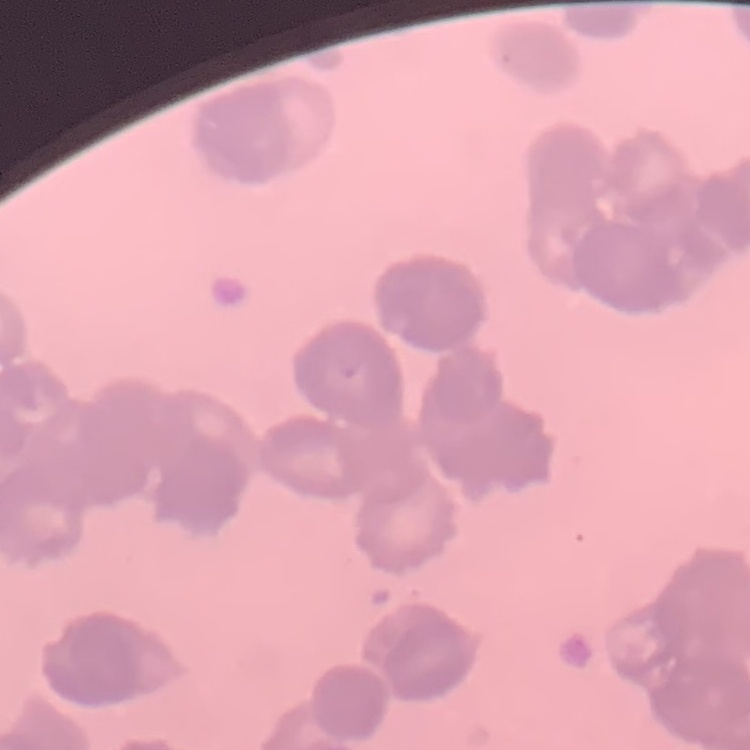 The red blood cells exhibit rouleaux formation. Thin blood film. One tile cut from a larger photomicrograph. Field's or Giemsa stain.